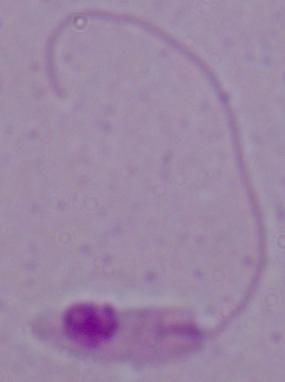
identification: Leishmania
magnification: 1000x
modality: photomicrograph